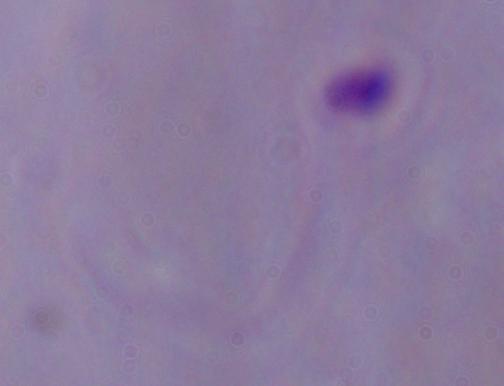
A Leishmania parasite is seen. Captured at 1000x magnification. Photomicrograph.